Locate every blood parasite and identify its species.
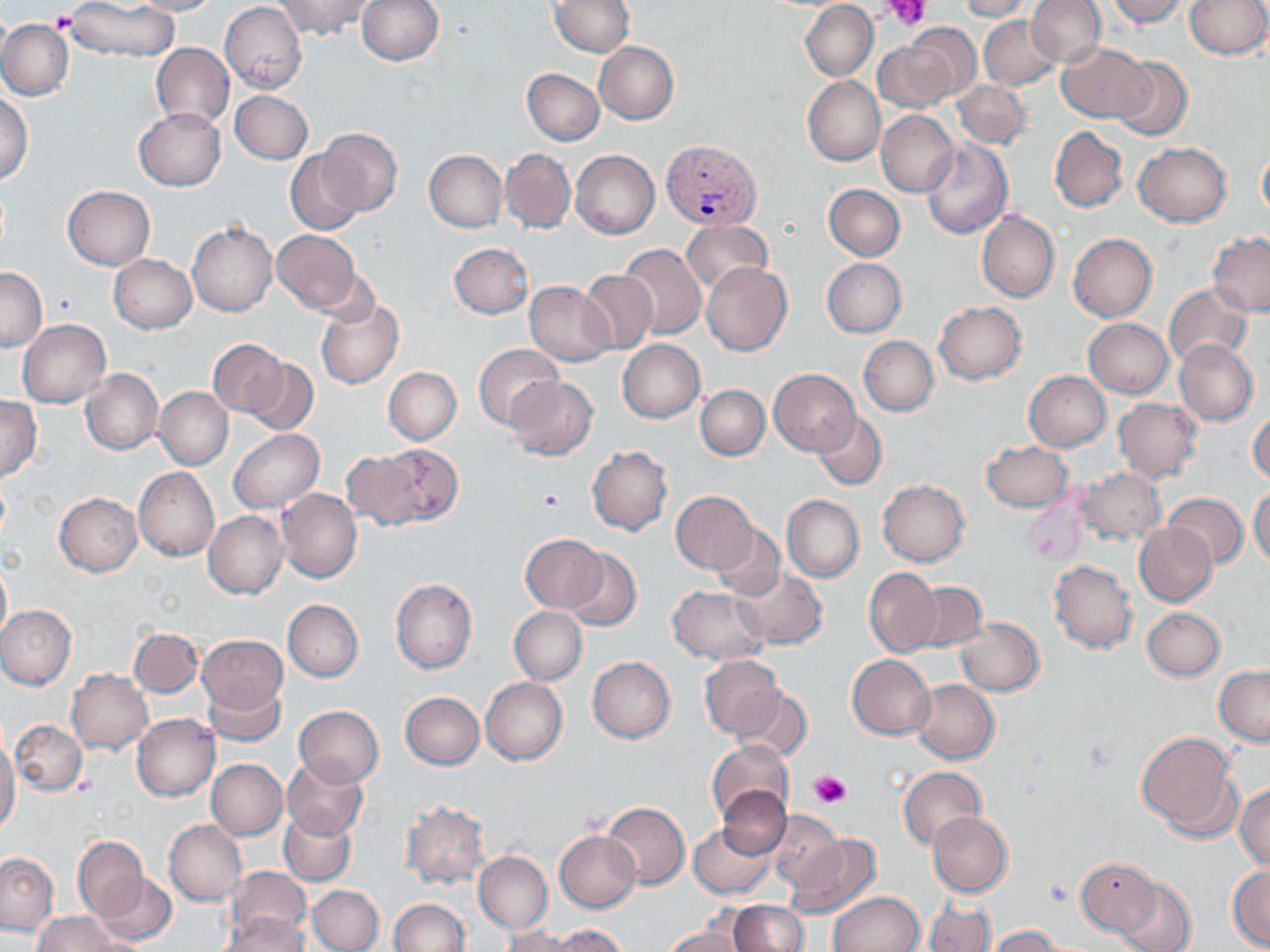
Approximate bounding boxes as named x1/y1/x2/y2 corners in pixels.
Plasmodium vivax-infected red blood cells: (x1=662, y1=140, x2=759, y2=228).
No Plasmodium falciparum, Plasmodium ovale, Plasmodium malariae, Babesia divergens, or Trypanosoma brucei observed.

Platelet locations: (x1=887, y1=0, x2=928, y2=28), (x1=48, y1=9, x2=78, y2=33), (x1=538, y1=488, x2=564, y2=512), (x1=811, y1=769, x2=850, y2=809). Uninfected red blood cell locations: (x1=128, y1=0, x2=223, y2=16), (x1=275, y1=0, x2=374, y2=40), (x1=357, y1=0, x2=445, y2=65), (x1=551, y1=0, x2=634, y2=56), (x1=958, y1=0, x2=1032, y2=21), (x1=1027, y1=0, x2=1106, y2=67), (x1=1106, y1=0, x2=1192, y2=28), (x1=1185, y1=0, x2=1270, y2=60), (x1=64, y1=1, x2=181, y2=63), (x1=220, y1=2, x2=306, y2=94), (x1=800, y1=2, x2=877, y2=81), (x1=979, y1=16, x2=1062, y2=89), (x1=0, y1=19, x2=72, y2=101), (x1=906, y1=23, x2=981, y2=101), (x1=872, y1=39, x2=956, y2=113), (x1=595, y1=42, x2=678, y2=124), (x1=151, y1=43, x2=234, y2=130), (x1=1057, y1=43, x2=1155, y2=122), (x1=1110, y1=55, x2=1193, y2=141), (x1=522, y1=68, x2=604, y2=144), (x1=804, y1=76, x2=885, y2=166), (x1=953, y1=80, x2=1033, y2=149), (x1=231, y1=90, x2=313, y2=163), (x1=0, y1=93, x2=32, y2=184), (x1=133, y1=108, x2=225, y2=190), (x1=877, y1=110, x2=958, y2=197), (x1=1050, y1=126, x2=1128, y2=213), (x1=316, y1=129, x2=403, y2=217), (x1=922, y1=139, x2=1012, y2=239), (x1=1134, y1=143, x2=1230, y2=227), (x1=1257, y1=145, x2=1270, y2=223), (x1=500, y1=148, x2=575, y2=234), (x1=286, y1=150, x2=365, y2=236), (x1=424, y1=150, x2=506, y2=231), (x1=571, y1=150, x2=659, y2=239), (x1=823, y1=184, x2=904, y2=261), (x1=63, y1=186, x2=155, y2=269), (x1=977, y1=211, x2=1058, y2=303), (x1=681, y1=219, x2=774, y2=294), (x1=188, y1=223, x2=277, y2=316), (x1=272, y1=230, x2=361, y2=314), (x1=1207, y1=232, x2=1270, y2=317), (x1=1069, y1=234, x2=1157, y2=322), (x1=449, y1=243, x2=533, y2=318), (x1=618, y1=243, x2=707, y2=340), (x1=109, y1=254, x2=197, y2=333), (x1=822, y1=258, x2=905, y2=337), (x1=702, y1=262, x2=792, y2=356), (x1=0, y1=266, x2=46, y2=351), (x1=579, y1=270, x2=658, y2=356), (x1=524, y1=281, x2=616, y2=366), (x1=1165, y1=284, x2=1253, y2=369), (x1=315, y1=297, x2=404, y2=390), (x1=934, y1=302, x2=1026, y2=385), (x1=1084, y1=318, x2=1174, y2=398), (x1=18, y1=320, x2=111, y2=406), (x1=859, y1=336, x2=938, y2=416), (x1=617, y1=339, x2=705, y2=423), (x1=207, y1=340, x2=287, y2=419), (x1=1174, y1=340, x2=1258, y2=427), (x1=474, y1=343, x2=560, y2=430), (x1=242, y1=357, x2=319, y2=434), (x1=384, y1=367, x2=461, y2=444), (x1=81, y1=369, x2=163, y2=455), (x1=769, y1=370, x2=859, y2=454), (x1=1025, y1=371, x2=1110, y2=451), (x1=504, y1=375, x2=597, y2=459), (x1=695, y1=385, x2=769, y2=460), (x1=156, y1=387, x2=232, y2=470), (x1=0, y1=396, x2=41, y2=482), (x1=1113, y1=398, x2=1203, y2=483), (x1=1249, y1=409, x2=1270, y2=483), (x1=812, y1=410, x2=887, y2=490), (x1=228, y1=430, x2=324, y2=513), (x1=981, y1=441, x2=1072, y2=511), (x1=377, y1=445, x2=463, y2=524), (x1=588, y1=445, x2=672, y2=536), (x1=342, y1=452, x2=426, y2=528), (x1=134, y1=467, x2=220, y2=561), (x1=1077, y1=468, x2=1164, y2=544), (x1=879, y1=479, x2=970, y2=565), (x1=54, y1=481, x2=217, y2=570), (x1=1249, y1=484, x2=1270, y2=566), (x1=277, y1=489, x2=362, y2=583), (x1=672, y1=491, x2=760, y2=572), (x1=55, y1=493, x2=142, y2=576), (x1=1164, y1=493, x2=1247, y2=568), (x1=781, y1=495, x2=863, y2=582), (x1=1022, y1=497, x2=1087, y2=565), (x1=204, y1=510, x2=288, y2=598), (x1=1134, y1=522, x2=1218, y2=606), (x1=712, y1=526, x2=786, y2=601), (x1=520, y1=535, x2=608, y2=612), (x1=563, y1=548, x2=641, y2=632), (x1=0, y1=558, x2=11, y2=647), (x1=1049, y1=560, x2=1138, y2=652), (x1=863, y1=567, x2=941, y2=658), (x1=731, y1=569, x2=827, y2=648), (x1=390, y1=578, x2=476, y2=674), (x1=912, y1=583, x2=988, y2=653), (x1=667, y1=585, x2=771, y2=664), (x1=282, y1=598, x2=363, y2=681), (x1=0, y1=605, x2=76, y2=689), (x1=509, y1=606, x2=587, y2=684), (x1=1142, y1=607, x2=1225, y2=680), (x1=955, y1=617, x2=1044, y2=696), (x1=129, y1=628, x2=203, y2=696), (x1=199, y1=634, x2=287, y2=713), (x1=848, y1=654, x2=935, y2=738), (x1=698, y1=655, x2=783, y2=740), (x1=588, y1=657, x2=676, y2=744), (x1=1214, y1=665, x2=1270, y2=746), (x1=67, y1=669, x2=153, y2=755), (x1=480, y1=677, x2=568, y2=764), (x1=204, y1=679, x2=286, y2=745), (x1=911, y1=680, x2=1000, y2=764), (x1=733, y1=686, x2=812, y2=762), (x1=400, y1=692, x2=484, y2=769), (x1=294, y1=705, x2=383, y2=786), (x1=133, y1=714, x2=220, y2=801), (x1=11, y1=721, x2=87, y2=794), (x1=1139, y1=731, x2=1240, y2=836), (x1=0, y1=735, x2=19, y2=836), (x1=708, y1=740, x2=794, y2=827), (x1=281, y1=756, x2=369, y2=841), (x1=206, y1=758, x2=288, y2=840), (x1=899, y1=767, x2=986, y2=851), (x1=1234, y1=783, x2=1270, y2=873), (x1=716, y1=786, x2=793, y2=860), (x1=601, y1=801, x2=690, y2=889), (x1=400, y1=802, x2=491, y2=889), (x1=765, y1=809, x2=845, y2=890), (x1=279, y1=812, x2=356, y2=885), (x1=928, y1=812, x2=1012, y2=897), (x1=164, y1=819, x2=246, y2=906), (x1=689, y1=823, x2=775, y2=898), (x1=554, y1=830, x2=641, y2=912), (x1=783, y1=834, x2=881, y2=918), (x1=73, y1=836, x2=147, y2=918), (x1=473, y1=851, x2=552, y2=934), (x1=0, y1=852, x2=58, y2=936), (x1=1074, y1=856, x2=1161, y2=938), (x1=1228, y1=866, x2=1270, y2=950), (x1=224, y1=870, x2=312, y2=947), (x1=93, y1=872, x2=176, y2=946), (x1=1115, y1=875, x2=1197, y2=952), (x1=308, y1=884, x2=384, y2=951), (x1=830, y1=892, x2=925, y2=952), (x1=388, y1=898, x2=470, y2=952), (x1=923, y1=898, x2=996, y2=952), (x1=727, y1=901, x2=809, y2=951), (x1=34, y1=910, x2=120, y2=952), (x1=217, y1=912, x2=311, y2=952), (x1=552, y1=925, x2=631, y2=952), (x1=989, y1=925, x2=1064, y2=951), (x1=500, y1=926, x2=583, y2=952), (x1=663, y1=927, x2=747, y2=952). Slide-level diagnosis: Plasmodium vivax. May-Grünwald-Giemsa stain. Captured at 1000x magnification. Optical microscopy. Single field of view. Thin blood film. Image is 1270×952 pixels.